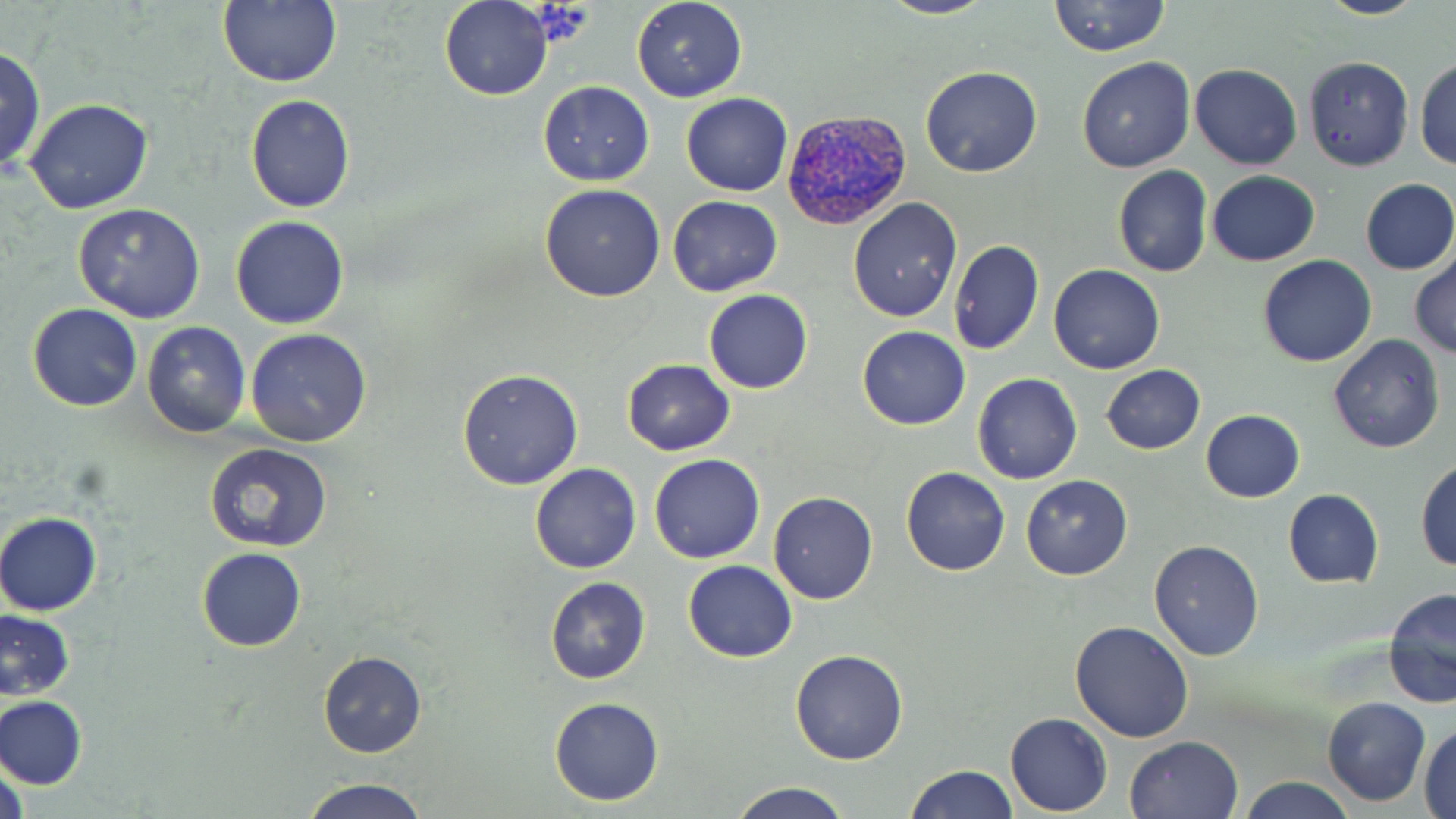
Summary:
  - Coordinate format: approximate bounding boxes as named x1/y1/x2/y2 corners in pixels
  - Plasmodium vivax-infected red blood cell locations: (x1=782, y1=107, x2=912, y2=234)
  - Uninfected red blood cell locations: (x1=219, y1=0, x2=342, y2=87), (x1=630, y1=0, x2=748, y2=102), (x1=876, y1=0, x2=996, y2=21), (x1=1048, y1=0, x2=1172, y2=56), (x1=1312, y1=0, x2=1433, y2=20), (x1=439, y1=1, x2=552, y2=101), (x1=0, y1=46, x2=46, y2=179), (x1=1415, y1=56, x2=1456, y2=169), (x1=1076, y1=57, x2=1197, y2=172), (x1=1302, y1=57, x2=1411, y2=170), (x1=1189, y1=63, x2=1301, y2=170), (x1=919, y1=66, x2=1042, y2=177), (x1=537, y1=82, x2=654, y2=184), (x1=680, y1=93, x2=792, y2=196), (x1=245, y1=94, x2=355, y2=212), (x1=24, y1=98, x2=154, y2=213), (x1=1113, y1=167, x2=1212, y2=278), (x1=1206, y1=170, x2=1321, y2=266), (x1=1358, y1=178, x2=1455, y2=276), (x1=539, y1=182, x2=666, y2=303), (x1=667, y1=196, x2=782, y2=295), (x1=846, y1=196, x2=961, y2=321), (x1=72, y1=202, x2=205, y2=322), (x1=230, y1=216, x2=350, y2=329), (x1=948, y1=240, x2=1044, y2=355), (x1=1409, y1=250, x2=1455, y2=359), (x1=1257, y1=254, x2=1376, y2=366), (x1=1047, y1=263, x2=1166, y2=374), (x1=704, y1=290, x2=813, y2=394), (x1=28, y1=304, x2=142, y2=411), (x1=141, y1=322, x2=250, y2=437), (x1=857, y1=326, x2=969, y2=430), (x1=245, y1=327, x2=373, y2=447), (x1=1327, y1=334, x2=1445, y2=454), (x1=621, y1=359, x2=735, y2=456), (x1=1102, y1=364, x2=1205, y2=453), (x1=457, y1=369, x2=583, y2=490), (x1=972, y1=373, x2=1081, y2=485), (x1=1200, y1=410, x2=1305, y2=503), (x1=205, y1=443, x2=331, y2=550), (x1=649, y1=453, x2=765, y2=564), (x1=1414, y1=458, x2=1456, y2=571), (x1=530, y1=462, x2=641, y2=574), (x1=901, y1=467, x2=1010, y2=577), (x1=1020, y1=474, x2=1133, y2=580), (x1=1282, y1=488, x2=1383, y2=588), (x1=768, y1=492, x2=878, y2=604), (x1=0, y1=511, x2=102, y2=616), (x1=1148, y1=537, x2=1264, y2=660), (x1=197, y1=547, x2=306, y2=652), (x1=683, y1=560, x2=796, y2=661), (x1=545, y1=576, x2=651, y2=684), (x1=1383, y1=588, x2=1456, y2=710), (x1=0, y1=608, x2=75, y2=700), (x1=1069, y1=621, x2=1194, y2=743), (x1=790, y1=648, x2=909, y2=765), (x1=318, y1=651, x2=427, y2=758), (x1=1321, y1=695, x2=1431, y2=806), (x1=1, y1=696, x2=87, y2=789), (x1=549, y1=697, x2=664, y2=804), (x1=1005, y1=713, x2=1112, y2=814), (x1=1419, y1=725, x2=1456, y2=819), (x1=1124, y1=735, x2=1243, y2=819), (x1=2, y1=756, x2=28, y2=819), (x1=901, y1=763, x2=1016, y2=819), (x1=1238, y1=776, x2=1357, y2=818), (x1=299, y1=777, x2=432, y2=819), (x1=726, y1=782, x2=855, y2=819)
  - Slide-level diagnosis: Plasmodium vivax
  - Stain: May-Grünwald-Giemsa
  - Magnification: 1000x
  - Preparation: thin blood film
  - Image size: 1456×819 pixels
  - Field of view: single
  - Modality: light microscopy